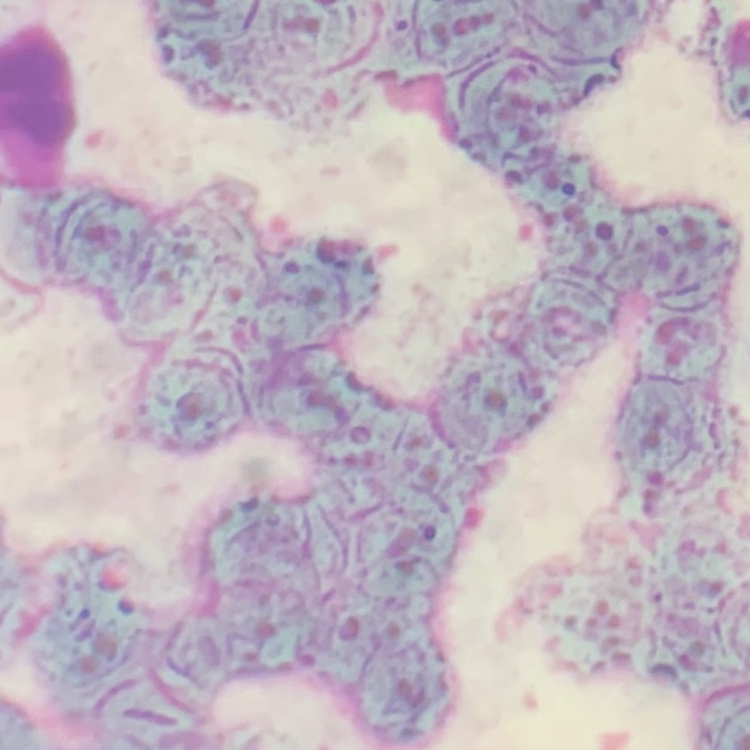

The red blood cells exhibit rouleaux formation. Field's or Giemsa stain. Thin blood film. Square crop of a larger photomicrograph.